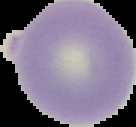

From a thin blood smear. Malaria status: uninfected. The area outside the segmented cell region is set to black. Image is 136×127 pixels.